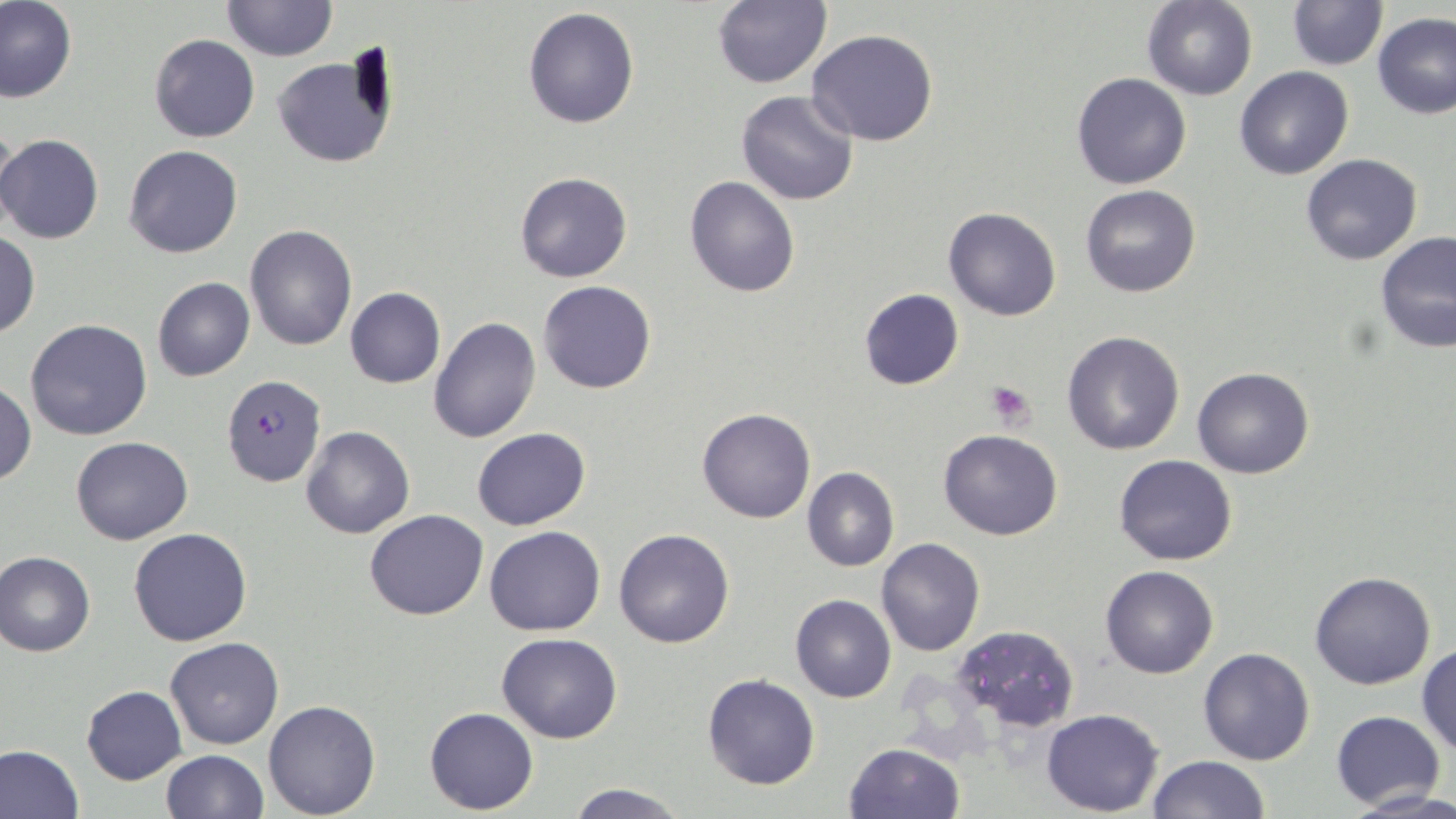

Summary:
  - Coordinate format: approximate bounding boxes as named x1/y1/x2/y2 corners in pixels
  - Uninfected red blood cell locations: (x1=0, y1=0, x2=78, y2=103), (x1=220, y1=0, x2=337, y2=63), (x1=1285, y1=0, x2=1389, y2=70), (x1=712, y1=1, x2=831, y2=88), (x1=1141, y1=1, x2=1257, y2=99), (x1=523, y1=6, x2=639, y2=129), (x1=1373, y1=14, x2=1456, y2=119), (x1=806, y1=28, x2=940, y2=146), (x1=148, y1=34, x2=260, y2=143), (x1=270, y1=51, x2=397, y2=168), (x1=1234, y1=66, x2=1356, y2=180), (x1=1072, y1=73, x2=1191, y2=190), (x1=735, y1=90, x2=859, y2=207), (x1=1, y1=118, x2=22, y2=235), (x1=0, y1=135, x2=104, y2=244), (x1=123, y1=145, x2=243, y2=259), (x1=1299, y1=154, x2=1423, y2=267), (x1=515, y1=172, x2=632, y2=284), (x1=684, y1=175, x2=800, y2=297), (x1=1079, y1=185, x2=1200, y2=298), (x1=942, y1=207, x2=1061, y2=321), (x1=244, y1=226, x2=357, y2=349), (x1=0, y1=232, x2=39, y2=339), (x1=1375, y1=232, x2=1456, y2=355), (x1=151, y1=277, x2=256, y2=382), (x1=537, y1=280, x2=656, y2=393), (x1=345, y1=288, x2=445, y2=390), (x1=858, y1=289, x2=963, y2=391), (x1=428, y1=317, x2=541, y2=444), (x1=24, y1=318, x2=154, y2=441), (x1=1061, y1=330, x2=1185, y2=455), (x1=1192, y1=367, x2=1315, y2=479), (x1=0, y1=381, x2=36, y2=486), (x1=697, y1=406, x2=817, y2=524), (x1=299, y1=426, x2=415, y2=540), (x1=471, y1=427, x2=592, y2=531), (x1=938, y1=428, x2=1062, y2=539), (x1=71, y1=436, x2=194, y2=545), (x1=1114, y1=454, x2=1237, y2=566), (x1=801, y1=467, x2=899, y2=571), (x1=365, y1=509, x2=488, y2=621), (x1=484, y1=526, x2=605, y2=636), (x1=129, y1=527, x2=253, y2=646), (x1=613, y1=528, x2=735, y2=648), (x1=875, y1=537, x2=986, y2=656), (x1=1, y1=552, x2=96, y2=658), (x1=1100, y1=565, x2=1219, y2=678), (x1=1309, y1=571, x2=1437, y2=690), (x1=790, y1=594, x2=895, y2=703), (x1=951, y1=623, x2=1080, y2=730), (x1=497, y1=633, x2=623, y2=743), (x1=166, y1=636, x2=285, y2=749), (x1=1416, y1=644, x2=1456, y2=757), (x1=1197, y1=647, x2=1318, y2=765), (x1=701, y1=675, x2=820, y2=791), (x1=80, y1=685, x2=186, y2=785), (x1=263, y1=700, x2=381, y2=818), (x1=425, y1=707, x2=538, y2=813), (x1=1041, y1=708, x2=1164, y2=815), (x1=1331, y1=709, x2=1445, y2=810), (x1=844, y1=743, x2=965, y2=819), (x1=0, y1=744, x2=86, y2=819), (x1=159, y1=749, x2=269, y2=819), (x1=1147, y1=754, x2=1272, y2=819), (x1=565, y1=781, x2=688, y2=818), (x1=1349, y1=788, x2=1456, y2=817)
  - Plasmodium falciparum-infected red blood cell locations: (x1=222, y1=374, x2=326, y2=486)
  - Platelet locations: (x1=984, y1=380, x2=1036, y2=428)
  - Slide-level diagnosis: Plasmodium falciparum
  - Image size: 1456×819 pixels
  - Magnification: 1000x
  - Stain: May-Grünwald-Giemsa
  - Field of view: one of a larger specimen
  - Preparation: thin blood smear
  - Modality: light microscopy